Assess the morphology of the red blood cells.
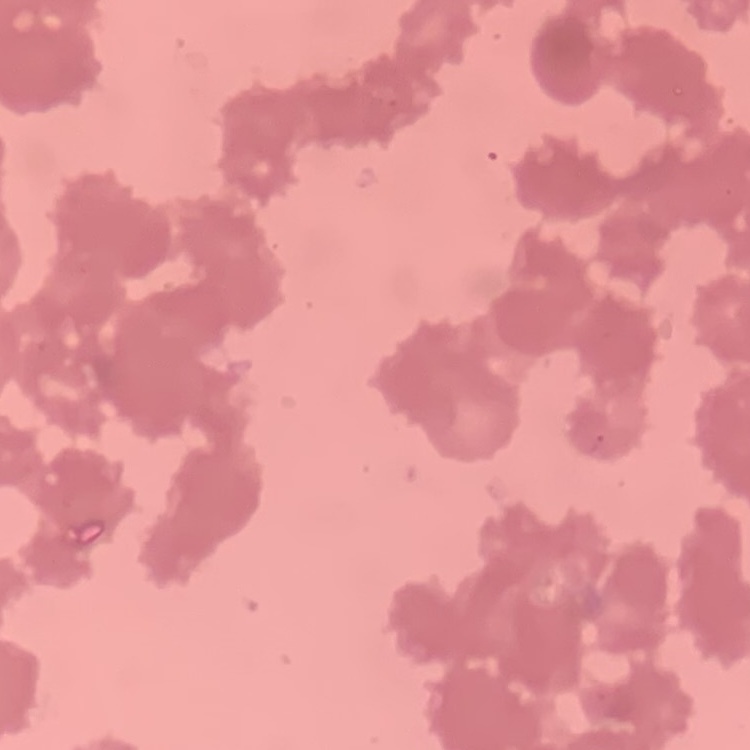

Rouleaux formation.

Thin peripheral smear. Square crop of a larger photomicrograph. Field's or Giemsa stain.